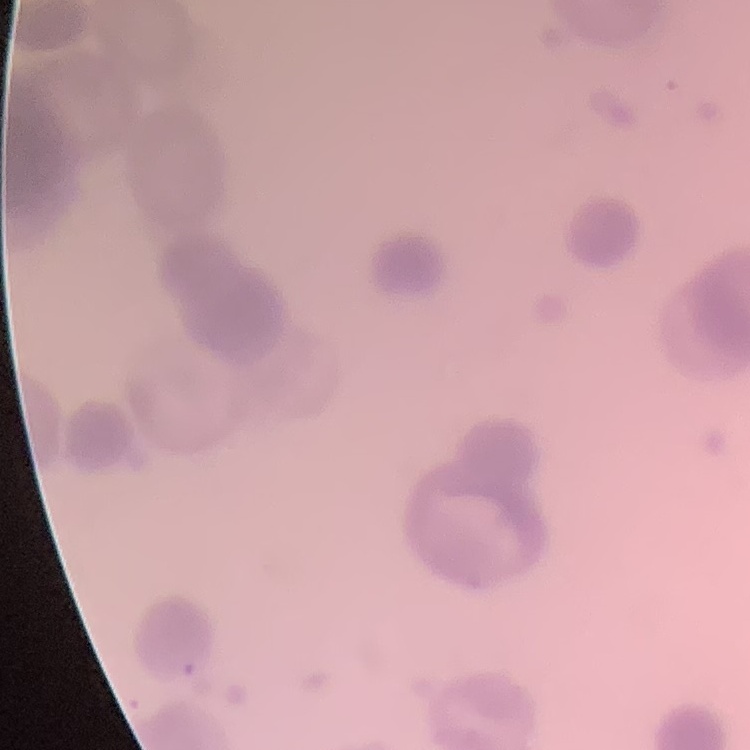
Summary:
  - Red blood cell morphology: rouleaux formation
  - Image type: one tile cut from a larger photomicrograph
  - Stain: Field's or Giemsa
  - Preparation: thin peripheral smear